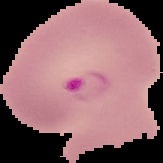
From a thin blood film. Result: malaria parasites identified. Cell region segmented out of the field of view; the surrounding area is masked to black. Image is 163×163 pixels.